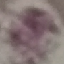
malaria status = uninfected
stain = Giemsa
image type = automatically extracted cell patch, resized to 64 × 64 pixels
capture = smartphone through the microscope eyepiece
preparation = thin blood smear